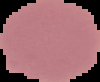
{
  "preparation": "thin blood film",
  "image_type": "segmented cell region with the area outside set to black",
  "malaria_status": "uninfected",
  "image_size": "100×82 pixels"
}